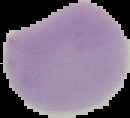

image size = 130×118 pixels
image type = segmented cell region with the area outside set to black
result = no Plasmodium parasites seen
preparation = thin blood film